Classify this cell by malaria status.
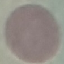
It is uninfected.

Acquired by smartphone through the microscope eyepiece. Cell patch, automatically extracted from a larger field of view and resized to 64 × 64 pixels. Giemsa stain. Thin blood film.